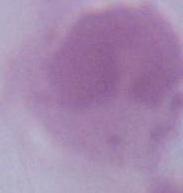
magnification = 1000x
identification = erythrocyte
modality = photomicrograph